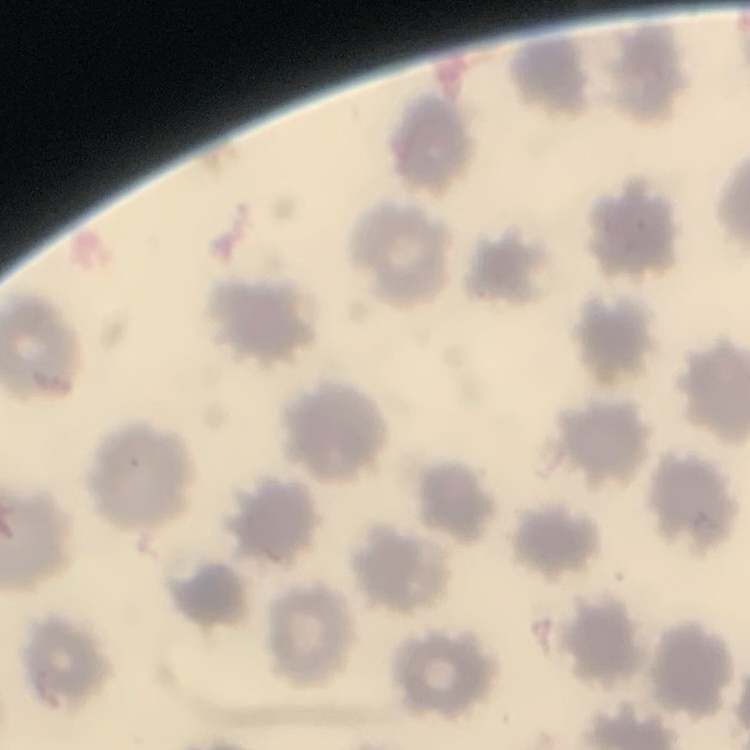
red blood cell morphology = no rouleaux formation
image type = one tile cut from a larger photomicrograph
stain = Field's or Giemsa
preparation = thin blood film